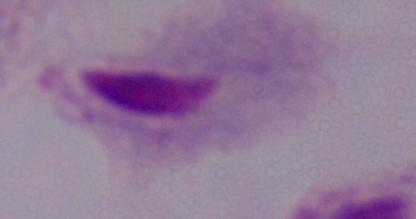

magnification = 1000x
identification = trichomonad
modality = micrograph